Assess the morphology of the erythrocytes.
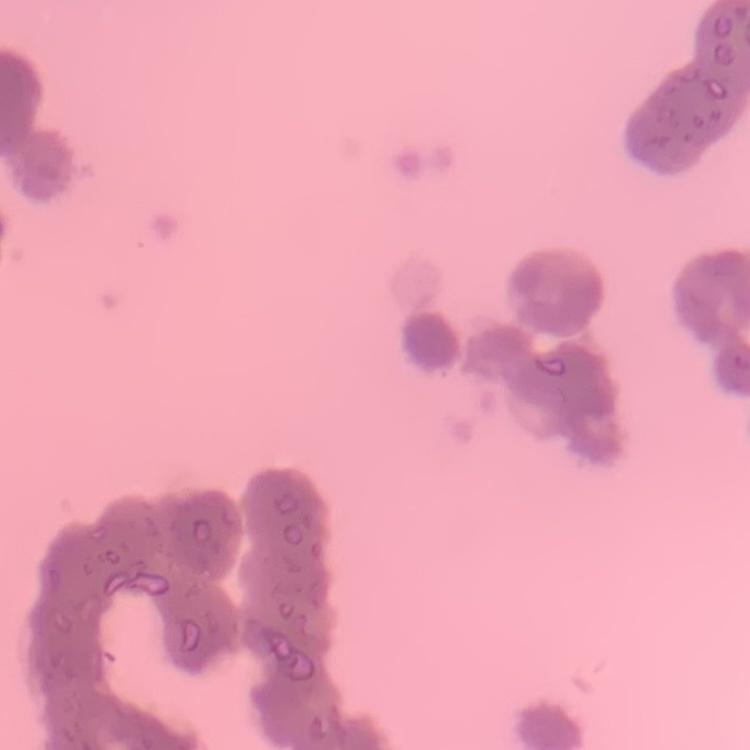

They show rouleaux formation.

Summary:
  - Image type: one tile cut from a larger photomicrograph
  - Stain: Field's or Giemsa
  - Preparation: thin blood film